Assess the morphology of the erythrocytes.
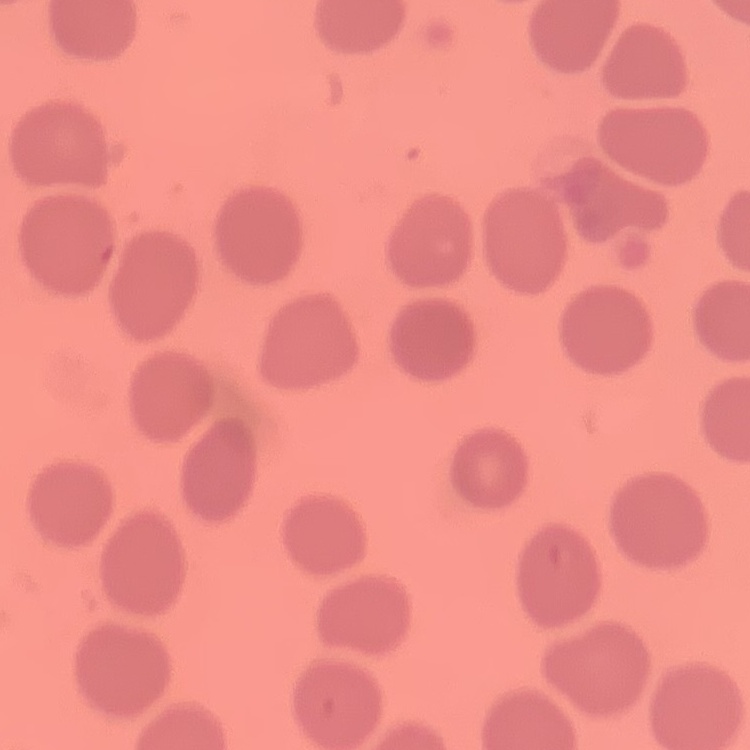

No rouleaux formation.

Thin blood smear. Square crop of a larger photomicrograph. Field's or Giemsa stain.